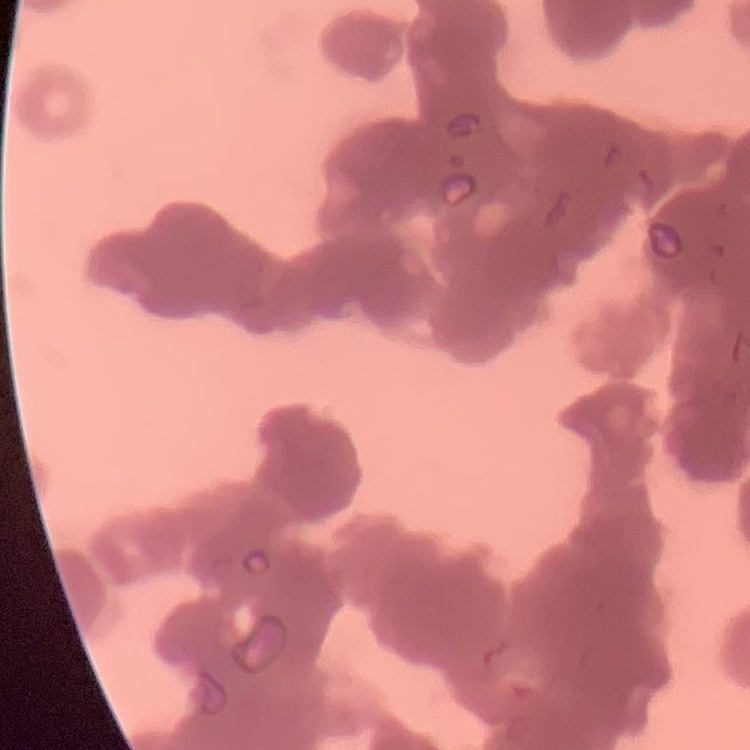
The erythrocytes show rouleaux formation. Thin blood smear. Stained with either Field's or Giemsa. Square crop of a larger photomicrograph.